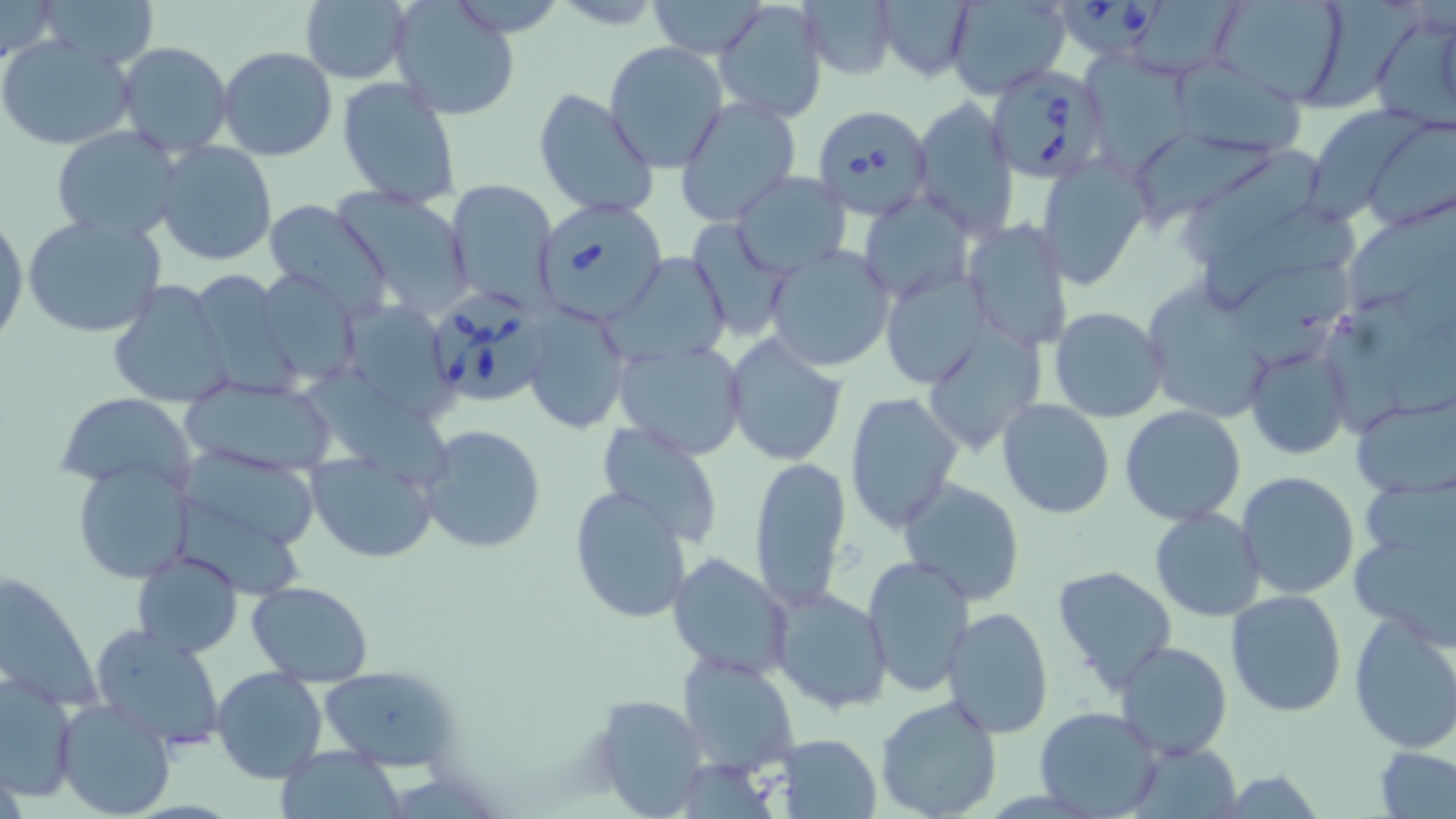

Approximate bounding boxes as (x1,y1)-(x2,y2) corner pairs in pixels. Uninfected red blood cell locations: (1,0)-(58,64), (36,0)-(157,70), (299,0)-(412,84), (646,0)-(770,58), (712,0)-(828,121), (874,0)-(976,83), (1215,0)-(1350,106), (799,1)-(899,81), (944,1)-(1070,97), (1312,2)-(1422,111), (390,3)-(520,121), (1366,9)-(1456,128), (1,35)-(136,150), (115,41)-(234,160), (605,42)-(728,172), (217,46)-(337,163), (1091,50)-(1200,181), (1173,60)-(1310,161), (336,76)-(462,209), (533,88)-(659,219), (675,97)-(802,225), (913,99)-(1019,235), (1310,113)-(1428,220), (1365,118)-(1456,231), (51,125)-(185,241), (1134,133)-(1290,224), (154,142)-(277,266), (1183,148)-(1318,259), (1037,157)-(1152,291), (733,173)-(849,276), (443,178)-(556,308), (329,187)-(477,318), (861,191)-(973,305), (265,201)-(393,321), (1346,204)-(1456,303), (1200,205)-(1363,303), (22,213)-(168,341), (0,215)-(27,345), (688,217)-(793,341), (962,218)-(1074,350), (765,244)-(895,372), (612,252)-(731,366), (1237,259)-(1355,369), (883,269)-(990,389), (259,273)-(371,380), (107,280)-(234,410), (1152,287)-(1275,416), (1325,291)-(1425,436), (351,302)-(461,422), (521,302)-(633,437), (1050,307)-(1168,423), (921,324)-(1047,451), (723,335)-(848,466), (1244,340)-(1352,460), (612,342)-(748,460), (293,369)-(461,483), (182,376)-(340,477), (845,392)-(962,532), (56,394)-(198,493), (1352,396)-(1455,495), (996,399)-(1115,519), (1119,405)-(1247,527), (417,421)-(547,555), (595,424)-(726,549), (172,447)-(322,541), (307,452)-(441,564), (747,456)-(853,614), (72,461)-(195,584), (1236,471)-(1360,598), (898,478)-(1025,608), (570,489)-(696,623), (175,492)-(315,599), (1150,507)-(1264,622), (1353,514)-(1456,643), (132,549)-(242,659), (667,553)-(794,681), (863,556)-(974,697), (1051,564)-(1179,694), (246,580)-(372,685), (770,586)-(893,715), (1226,589)-(1347,718), (942,606)-(1053,740), (1348,608)-(1456,755), (89,623)-(228,751), (1115,640)-(1234,760), (677,653)-(799,777), (315,664)-(455,771), (211,667)-(327,783), (1,676)-(79,804), (599,693)-(703,813), (874,696)-(1004,819), (55,698)-(176,819), (1035,706)-(1163,816), (772,733)-(884,818), (1376,744)-(1456,817), (274,747)-(404,816). Babesia divergens-infected red blood cell locations: (1063,0)-(1164,59), (987,64)-(1112,185), (812,103)-(934,219), (536,199)-(670,317), (426,289)-(552,401). Slide-level diagnosis: Babesia divergens. May-Grünwald-Giemsa stain. 1000x magnification. Thin blood smear. Light microscopy. Single field of view. Image is 1456×819 pixels.